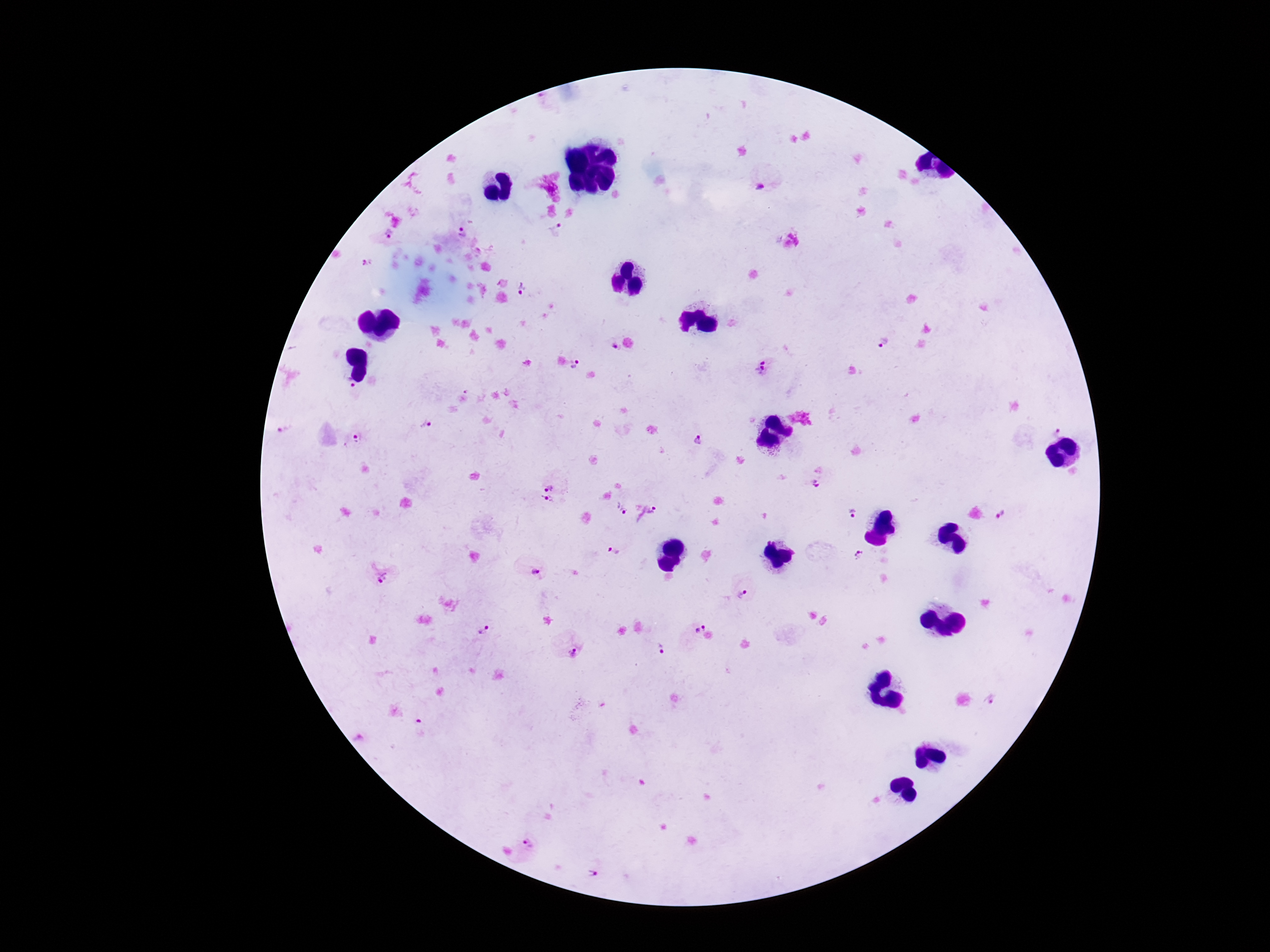
Approximate centers as (x, y) in pixels.
Summary:
  - Plasmodium parasite locations: (762, 186), (461, 230), (556, 230), (390, 235), (366, 264), (522, 290), (882, 343), (611, 346), (575, 364), (764, 366), (346, 385), (425, 424), (1058, 431), (284, 434), (356, 439), (697, 441), (817, 484), (550, 485), (546, 503), (621, 510), (852, 513), (647, 515), (1006, 516), (615, 553), (860, 555), (534, 571), (382, 578), (745, 595), (699, 627), (484, 630), (660, 650), (572, 651), (992, 700), (528, 847), (592, 872)
  - Capture: smartphone camera through the microscope eyepiece
  - Magnification: 100x
  - Preparation: thick blood smear
  - Patient malaria status: infected
  - Image size: 1270×952 pixels
  - Stain: Giemsa
  - Field of view: single